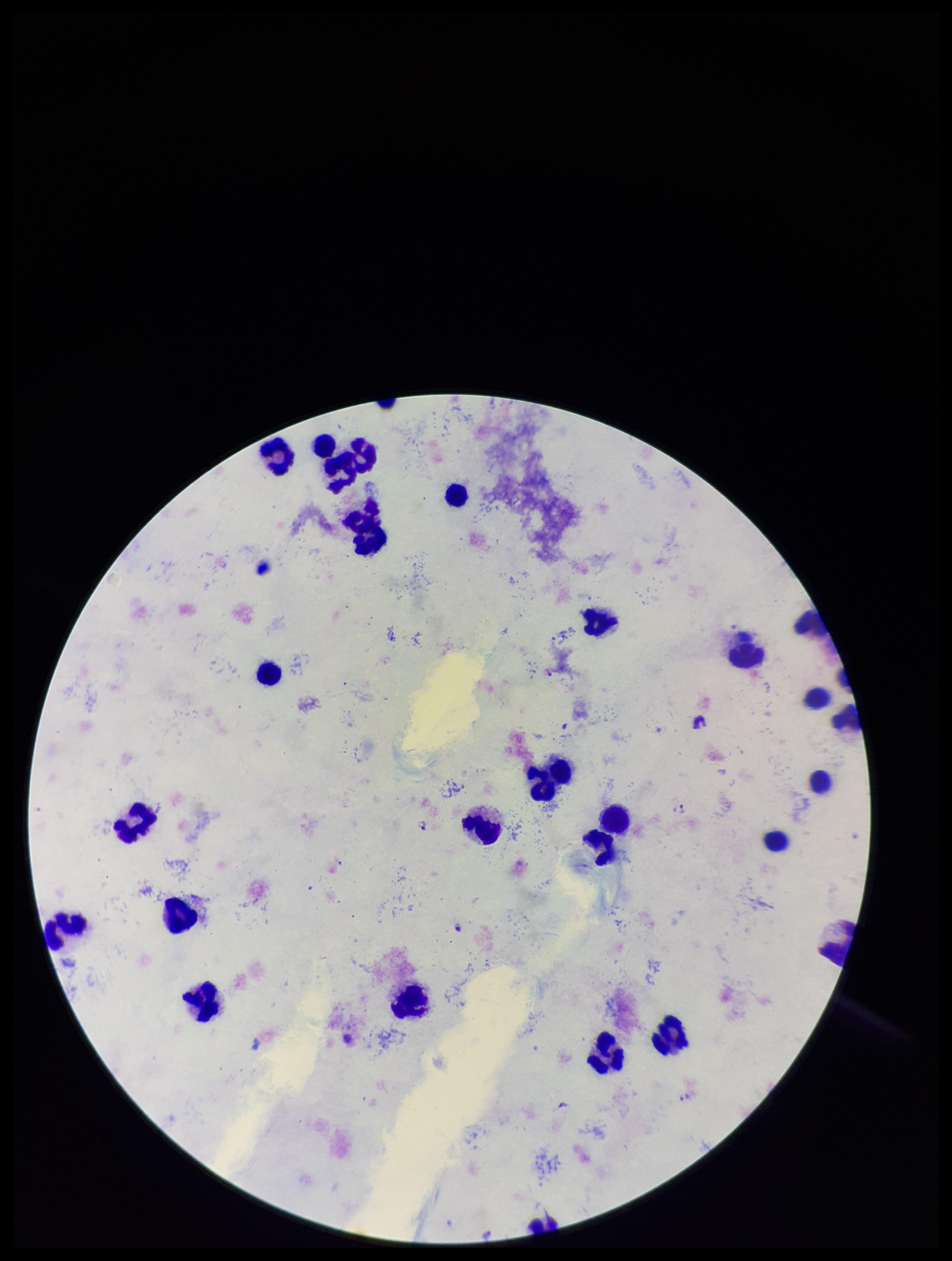

parasite count = 3
patient malaria status = infected
Plasmodium parasites = identified
field of view = one from this slide
leukocyte count = 27
capture = smartphone photograph through the microscope eyepiece
image size = 952×1261 pixels
species reported for this patient = Plasmodium falciparum
preparation = thick smear
stain = Giemsa